Classify this cell by malaria status.
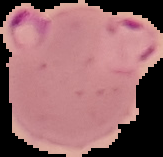
It is parasitized.

Image is 163×157 pixels. From a thin blood film. Cell region segmented out of the field of view; the surrounding area is masked to black.